Locate every Plasmodium malariae-infected red blood cell.
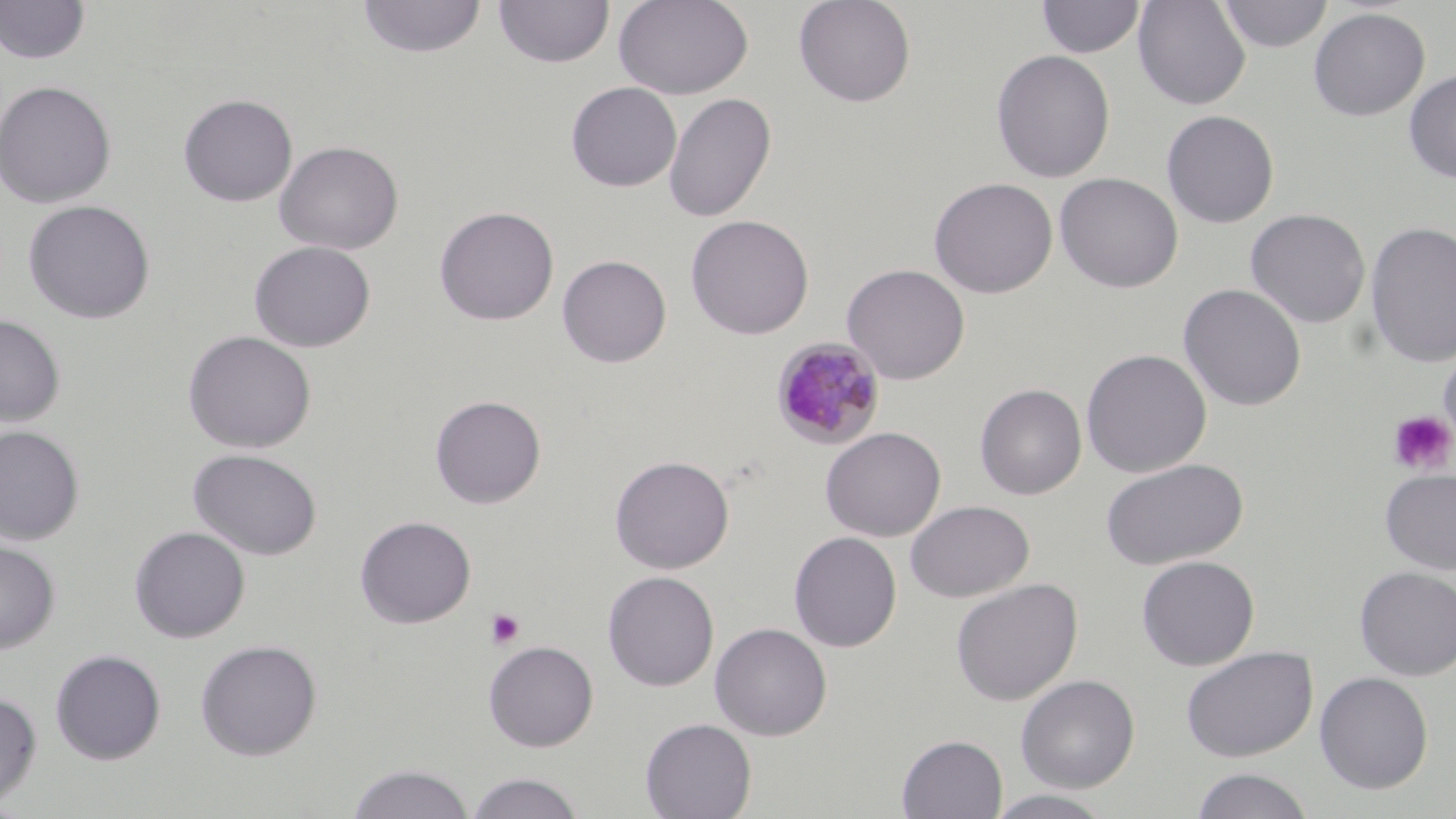
Approximate bounding boxes as (x1,y1)-(x2,y2) corner pairs in pixels.
Plasmodium malariae-infected red blood cells: (771,336)-(886,450).

Summary:
  - Uninfected red blood cell locations: (357,0)-(487,59), (493,0)-(614,68), (613,0)-(753,100), (793,0)-(917,107), (1037,0)-(1145,59), (1132,0)-(1251,110), (1218,0)-(1333,53), (1,1)-(90,65), (1308,7)-(1430,121), (991,49)-(1116,183), (1403,69)-(1456,184), (0,79)-(117,208), (566,81)-(682,192), (664,92)-(776,223), (178,93)-(297,207), (1161,109)-(1280,228), (275,140)-(404,255), (1055,172)-(1183,293), (928,177)-(1058,298), (22,199)-(156,324), (434,206)-(559,326), (1245,207)-(1371,328), (685,214)-(814,340), (1364,221)-(1456,368), (248,240)-(376,353), (557,255)-(671,368), (841,263)-(971,385), (1178,283)-(1307,412), (0,314)-(65,428), (182,330)-(317,454), (1438,342)-(1456,457), (1080,348)-(1212,478), (974,383)-(1087,500), (430,395)-(546,509), (0,425)-(84,546), (820,426)-(946,542), (187,448)-(323,561), (609,454)-(735,574), (1100,458)-(1249,570), (1380,468)-(1456,575), (905,500)-(1034,602), (354,515)-(476,628), (129,525)-(250,643), (788,531)-(902,652), (0,540)-(60,654), (1136,554)-(1260,670), (1354,566)-(1456,681), (602,570)-(719,692), (950,578)-(1083,706), (710,622)-(832,741), (195,638)-(322,760), (483,640)-(599,752), (1181,645)-(1318,762), (49,649)-(166,764), (1314,671)-(1434,794), (1016,674)-(1140,793), (0,691)-(42,808), (639,717)-(757,819), (896,734)-(1007,818), (346,763)-(476,819), (1190,767)-(1315,819), (464,771)-(587,818), (984,789)-(1115,818)
  - Platelet locations: (1388,409)-(1456,476), (486,608)-(525,649)
  - Slide-level diagnosis: Plasmodium malariae
  - Magnification: 1000x
  - Image size: 1456×819 pixels
  - Modality: optical microscopy
  - Stain: May-Grünwald-Giemsa
  - Field of view: single
  - Preparation: thin blood film